Give the position of every malaria parasite and every leukocyte.
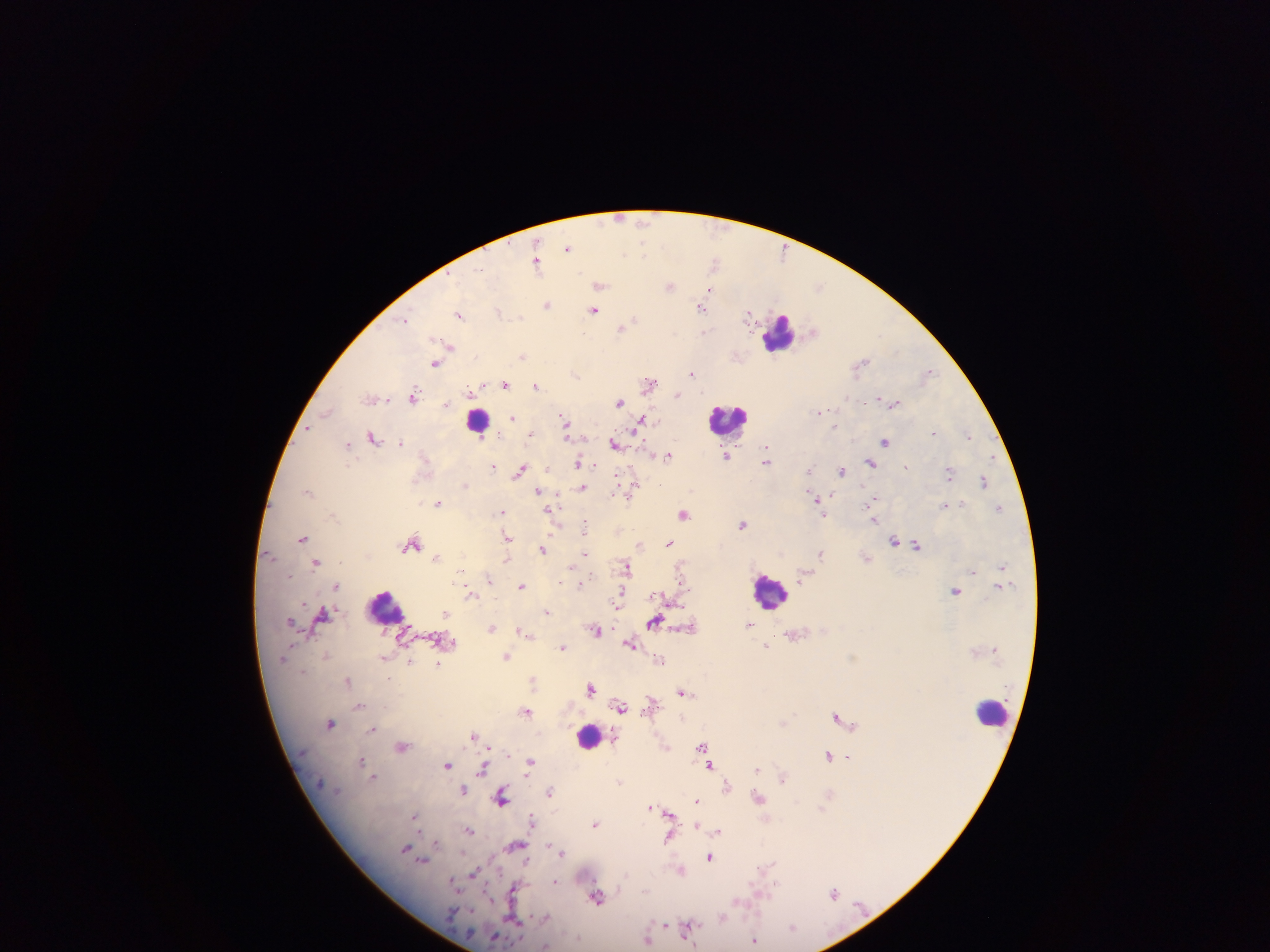
Approximate centers as [x, y] in pixels.
Malaria parasites: [644, 222], [567, 247], [643, 248], [624, 255], [714, 261], [537, 264], [600, 285], [669, 286], [819, 286], [710, 290], [547, 304], [701, 308], [594, 310], [499, 311], [748, 314], [460, 315], [405, 318], [633, 320], [622, 327], [813, 330], [705, 331], [450, 346], [523, 356], [861, 362], [435, 363], [928, 372], [576, 373], [692, 373], [649, 383], [505, 384], [475, 386], [536, 386], [678, 395], [413, 396], [371, 399], [619, 401], [894, 403], [446, 404], [327, 412], [821, 412], [511, 417], [565, 421], [642, 421], [834, 426], [308, 428], [934, 432], [531, 434], [567, 435], [968, 436], [374, 437], [886, 441], [401, 443], [615, 443], [347, 444], [767, 451], [668, 455], [727, 456], [767, 461], [579, 463], [870, 463], [493, 467], [905, 467], [520, 470], [809, 470], [842, 470], [949, 474], [984, 481], [464, 485], [633, 486], [582, 488], [308, 491], [538, 491], [814, 498], [874, 499], [438, 503], [818, 503], [962, 504], [945, 505], [549, 509], [999, 509], [502, 512], [683, 513], [823, 514], [873, 518], [742, 524], [585, 526], [508, 537], [302, 538], [894, 540], [411, 544], [640, 544], [668, 544], [917, 545], [542, 549], [821, 553], [585, 554], [436, 557], [316, 563], [626, 566], [1002, 566], [461, 570], [972, 572], [802, 577], [489, 579], [335, 585], [580, 585], [521, 586], [955, 590], [470, 593], [619, 597], [659, 598], [547, 612], [323, 613], [292, 621], [654, 622], [749, 625], [491, 628], [689, 628], [596, 631], [522, 632], [527, 634], [630, 644], [766, 646], [563, 647], [326, 655], [506, 657], [659, 660], [409, 662], [438, 664], [347, 680], [533, 680], [591, 689], [684, 692], [650, 703], [359, 705], [620, 707], [527, 712], [836, 716], [330, 723], [785, 723], [373, 728], [475, 735], [402, 746], [703, 746], [666, 747], [705, 754], [828, 755], [848, 756], [361, 761], [531, 763], [446, 765], [711, 766], [483, 769], [757, 769], [373, 776], [783, 777], [619, 782], [727, 786], [463, 790], [550, 792], [502, 798], [758, 798], [697, 800], [651, 807], [823, 807], [671, 813], [415, 818], [533, 820], [595, 823], [696, 825], [468, 830], [718, 831], [668, 838], [436, 844], [516, 846], [406, 848], [563, 852], [711, 858], [422, 860], [769, 865], [680, 870], [473, 873], [555, 881], [453, 882], [775, 884], [514, 890], [834, 892], [597, 896], [514, 918], [722, 918], [665, 924], [689, 927], [793, 927], [647, 938], [755, 941], [546, 946].
Leukocytes: [780, 332], [479, 419], [729, 419], [769, 590], [389, 609], [992, 713], [589, 737].

image size = 1270×952 pixels
country = Ghana
capture = mobile-phone photograph through a microscope
preparation = thick blood smear
field of view = single